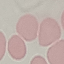
malaria status = uninfected
image type = automatically extracted cell patch, resized to 64 × 64 pixels
preparation = thin blood smear
capture = smartphone through the microscope eyepiece
stain = Giemsa